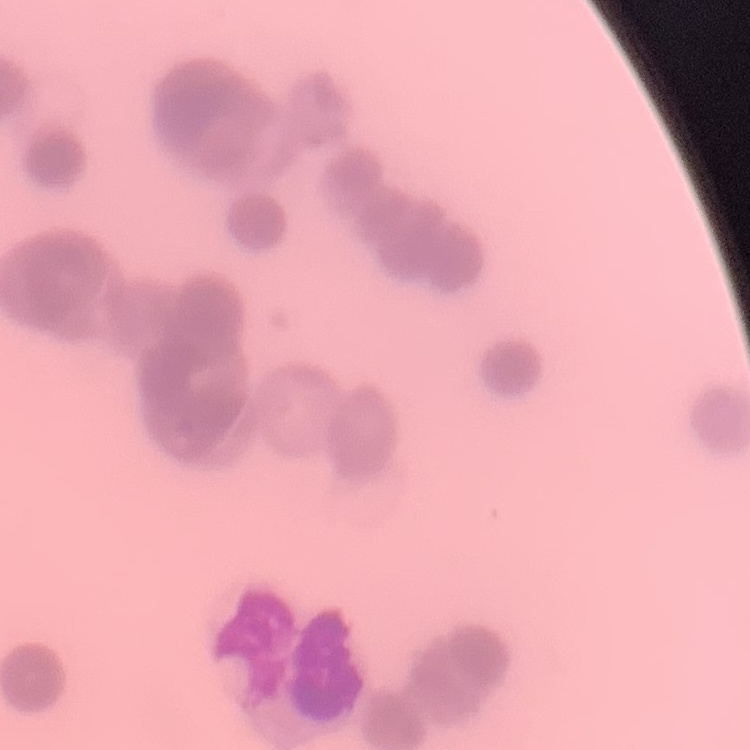
The red blood cells show rouleaux formation. Thin blood smear. Square crop of a larger photomicrograph. Stained with either Field's or Giemsa.